Locate every Plasmodium parasite and every leukocyte.
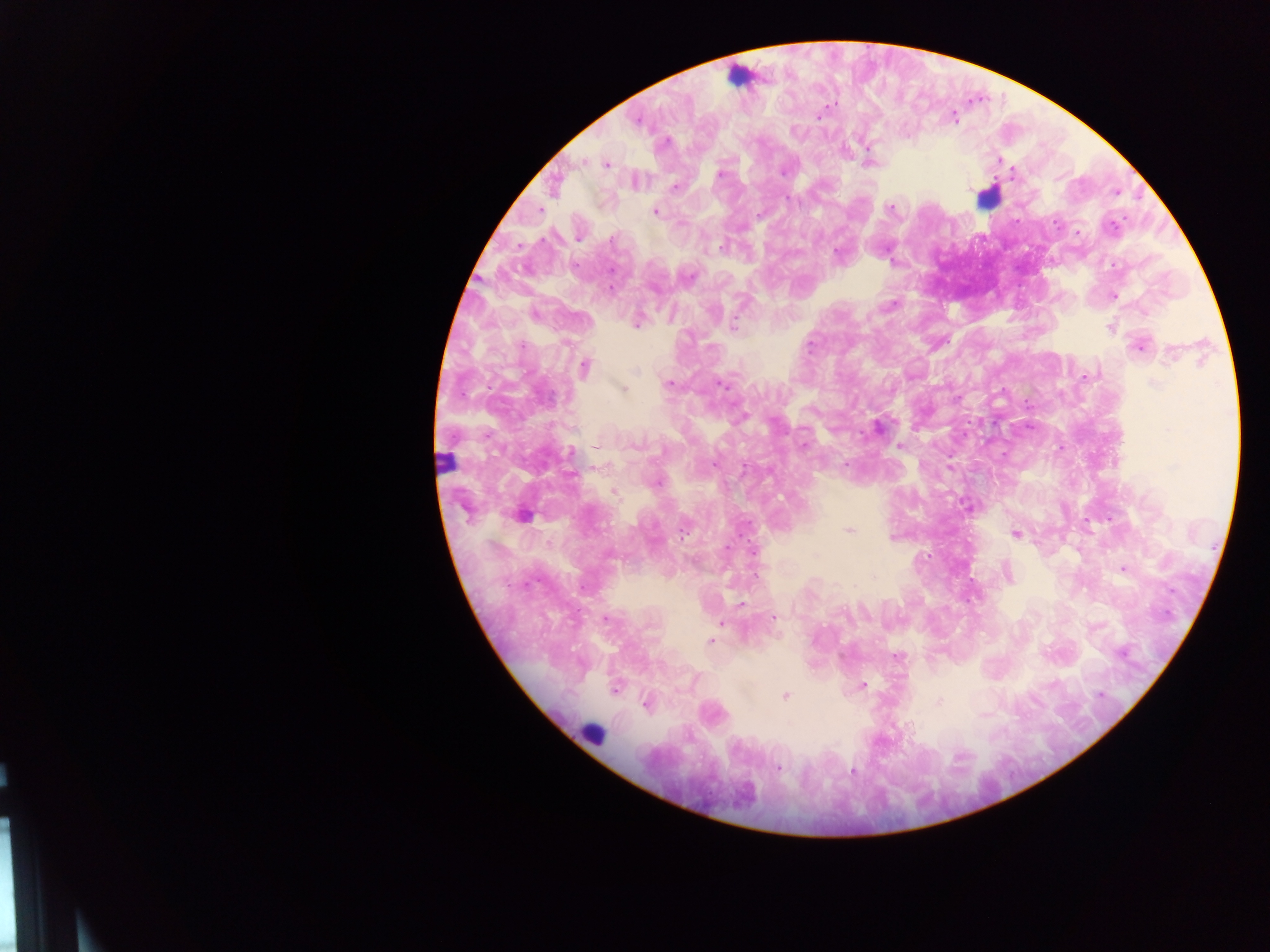

Approximate centers as (x, y) in pixels.
Plasmodium parasites: (833, 104), (819, 116), (954, 118), (636, 121), (666, 142), (998, 161), (582, 162), (606, 165), (782, 172), (1013, 173), (719, 174), (675, 188), (789, 198), (891, 209), (656, 212), (758, 215), (1056, 223), (1112, 227), (1077, 232), (578, 237), (612, 238), (722, 246), (837, 254), (892, 260), (689, 277), (611, 288), (1113, 296), (890, 306), (534, 315), (636, 324), (733, 325), (1110, 328), (811, 345), (523, 346), (1139, 346), (1171, 355), (585, 367), (635, 371), (1086, 376), (669, 383), (1155, 383), (720, 384), (622, 389), (957, 398), (741, 416), (877, 427), (1029, 428), (595, 446), (634, 446), (805, 446), (900, 446), (1060, 447), (571, 453), (1003, 455), (714, 464), (845, 464), (656, 482), (613, 492), (849, 530), (684, 532), (1016, 533), (891, 538), (727, 547), (753, 552), (1123, 569), (1008, 573), (742, 604), (773, 618), (605, 619), (720, 623), (711, 641), (1121, 653), (897, 656), (863, 685), (615, 690), (1100, 695), (784, 696), (939, 701), (647, 704), (778, 768), (852, 771).
Leukocytes: (987, 198), (444, 461), (517, 518), (592, 732).

country = Ghana
field of view = single
capture = mobile-phone photograph through a microscope
image size = 1270×952 pixels
preparation = thick blood film